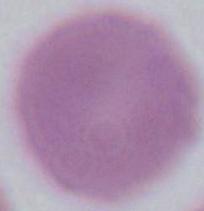
Summary:
  - Identification: erythrocyte
  - Magnification: 1000x
  - Modality: micrograph